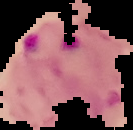
Image is 133×130 pixels. Result: malaria parasites identified. Cell region segmented out of the field of view; the surrounding area is masked to black. From a thin blood smear.